Identify the parasite.
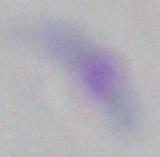

This is Toxoplasma gondii.

Summary:
  - Magnification: 1000x
  - Modality: photomicrograph